Assess this cell for malaria.
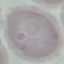

It is uninfected.

Giemsa stain. Thin blood smear. Cell patch, automatically extracted from a larger field of view and resized to 64 × 64 pixels. Acquired by smartphone through the microscope eyepiece.